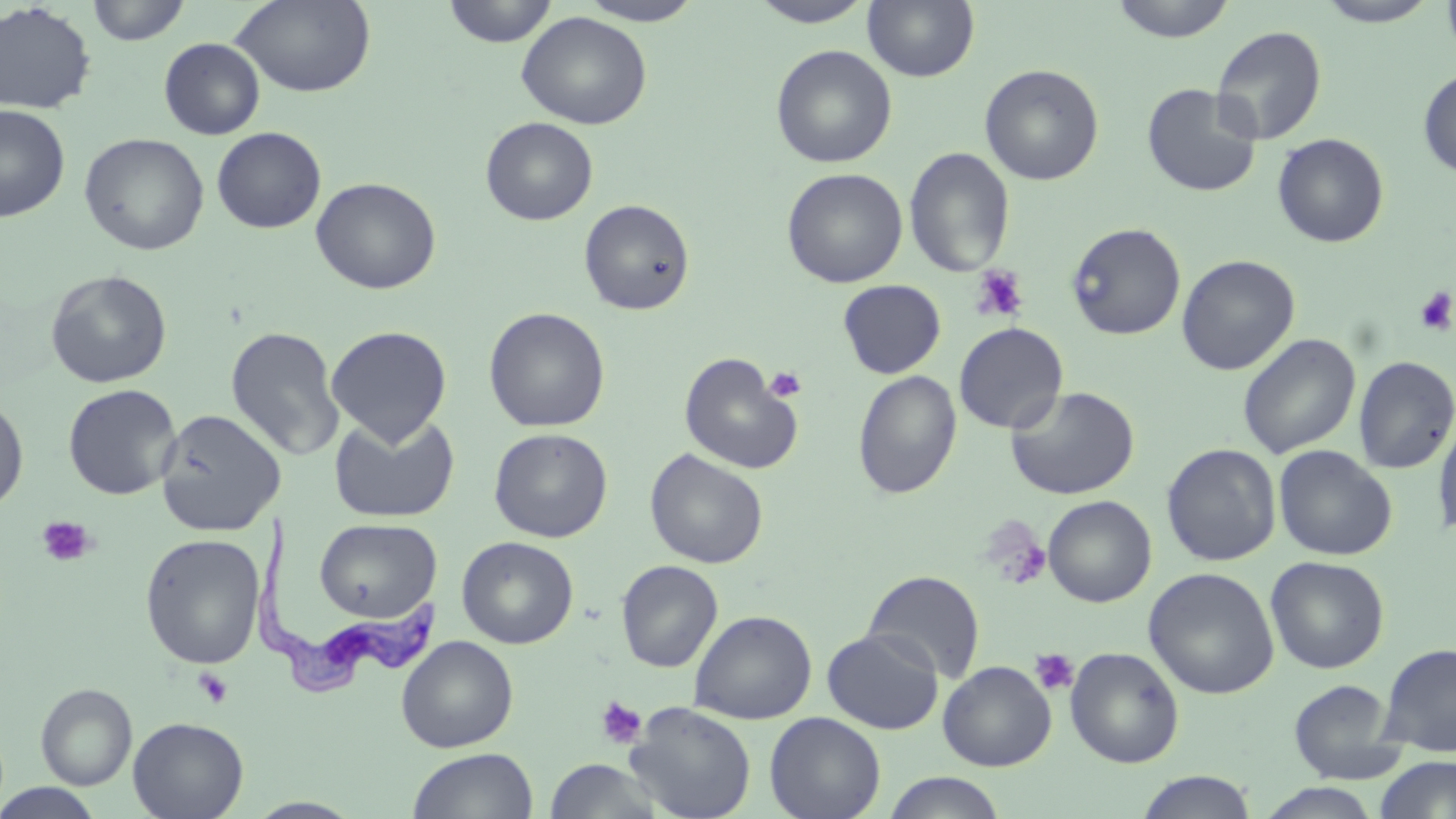
Trypanosoma brucei locations = approximate bounding boxes as [x1, y1, x2, y2] in pixels: [252, 510, 442, 695]
slide-level diagnosis = Trypanosoma brucei
preparation = thin blood smear
magnification = 1000x
platelet locations = approximate bounding boxes as [x1, y1, x2, y2] in pixels: [969, 265, 1029, 323], [1414, 287, 1456, 335], [764, 367, 807, 402], [37, 516, 95, 567], [981, 516, 1053, 590], [1029, 648, 1080, 697], [193, 668, 234, 709], [595, 695, 647, 749]
stain = May-Grünwald-Giemsa
modality = optical microscopy
image size = 1456×819 pixels
field of view = one of a larger specimen
uninfected red blood cell locations = approximate bounding boxes as [x1, y1, x2, y2] in pixels: [85, 0, 191, 46], [230, 0, 377, 97], [442, 0, 558, 48], [576, 0, 706, 25], [863, 0, 979, 82], [1107, 0, 1239, 42], [1314, 0, 1444, 27], [1441, 0, 1456, 64], [747, 1, 877, 27], [0, 2, 96, 114], [516, 11, 652, 130], [1211, 25, 1327, 145], [158, 37, 266, 140], [770, 44, 897, 168], [979, 63, 1104, 186], [1417, 66, 1456, 179], [1141, 82, 1262, 197], [0, 103, 71, 223], [481, 117, 598, 226], [211, 126, 326, 233], [78, 132, 210, 255], [1272, 133, 1389, 248], [904, 147, 1016, 277], [781, 168, 907, 288], [310, 176, 441, 295], [578, 199, 695, 315], [1066, 221, 1186, 341], [1176, 254, 1300, 376], [45, 270, 172, 388], [837, 280, 946, 378], [483, 306, 611, 433], [954, 322, 1069, 434], [325, 325, 452, 445], [225, 326, 345, 462], [1237, 333, 1361, 460], [678, 352, 804, 475], [1353, 355, 1456, 474], [852, 370, 962, 499], [62, 383, 182, 500], [1006, 385, 1140, 500], [0, 394, 29, 514], [1433, 407, 1456, 545], [154, 408, 286, 537], [328, 411, 460, 524], [489, 428, 613, 542], [1161, 443, 1282, 566], [1273, 445, 1397, 561], [644, 448, 769, 569], [1042, 495, 1157, 608], [315, 517, 441, 623], [140, 533, 266, 670], [456, 536, 578, 649], [1265, 555, 1389, 674], [616, 560, 723, 673], [1143, 567, 1280, 700], [863, 570, 986, 683], [689, 609, 817, 724], [822, 629, 943, 734], [396, 635, 518, 753], [1377, 641, 1456, 758], [1065, 646, 1184, 768], [938, 661, 1056, 771], [1289, 679, 1403, 783], [36, 683, 137, 789], [624, 702, 757, 819], [764, 712, 886, 819], [128, 717, 249, 819], [407, 747, 538, 818], [1375, 756, 1456, 819], [543, 759, 667, 818], [1134, 770, 1259, 818], [882, 771, 1007, 819], [0, 783, 105, 818], [1257, 783, 1385, 819]